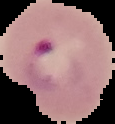

image_size: 115×124 pixels
preparation: thin blood smear
result: malaria parasites detected
image_type: segmented cell region with the area outside set to black